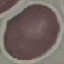
Summary:
  - Result: negative for malaria parasites
  - Image type: cell patch, automatically extracted from a larger field of view and resized to 64 × 64 pixels
  - Capture: smartphone through the microscope eyepiece
  - Preparation: thin smear
  - Stain: Giemsa